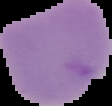

preparation = thin blood film
malaria status = uninfected
image type = segmented cell region on a black background
image size = 112×106 pixels